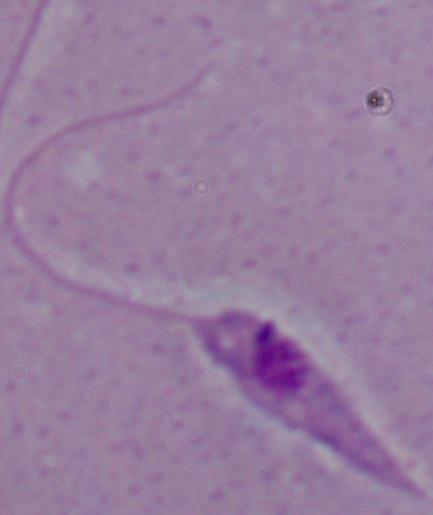
Summary:
  - Identification: Leishmania
  - Magnification: 1000x
  - Modality: photomicrograph